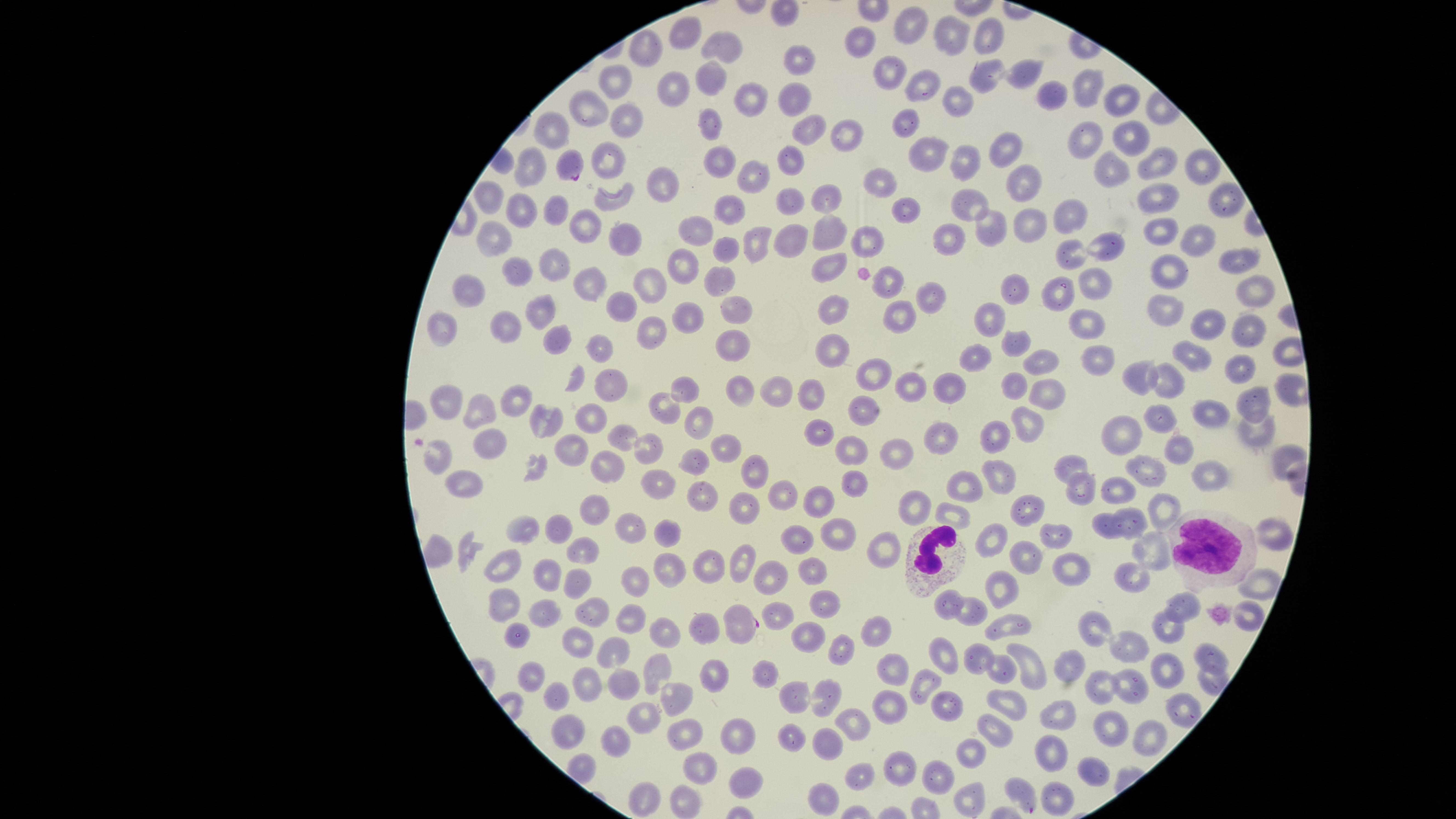

Approximate marker points as [x, y] in pixels.
Summary:
  - Parasitized RBCs: [565, 169], [741, 623]
  - Uninfected RBCs: [912, 22], [682, 33], [952, 35], [987, 35], [725, 39], [867, 41], [646, 50], [801, 56], [897, 71], [1026, 74], [985, 77], [711, 78], [619, 80], [920, 82], [674, 85], [1083, 91], [753, 95], [793, 96], [1054, 96], [1124, 98], [955, 100], [591, 107], [623, 115], [712, 123], [909, 123], [806, 129], [846, 130], [552, 134], [1087, 137], [1126, 137], [1005, 145], [925, 152], [608, 157], [789, 157], [723, 159], [963, 161], [1150, 163], [533, 164], [1108, 166], [1192, 166], [753, 174], [882, 177], [667, 184], [1022, 184], [1219, 193], [793, 194], [490, 197], [1156, 197], [908, 199], [618, 200], [731, 202], [826, 202], [970, 202], [527, 207], [1066, 212], [556, 218], [1028, 221], [586, 223], [990, 224], [695, 229], [828, 231], [953, 231], [1161, 231], [873, 234], [754, 237], [627, 238], [795, 239], [1197, 241], [497, 242], [1108, 243], [725, 248], [1072, 250], [1238, 257], [548, 265], [680, 265], [829, 266], [1167, 266], [515, 268], [719, 279], [888, 280], [591, 282], [652, 282], [1095, 283], [474, 287], [1023, 287], [1060, 288], [1252, 288], [930, 292], [624, 301], [834, 302], [730, 304], [1165, 308], [689, 310], [895, 310], [542, 315], [506, 317], [998, 317], [1089, 320], [1206, 320], [441, 324], [1246, 324], [651, 333], [563, 338], [734, 339], [1014, 345], [607, 347], [833, 347], [977, 352], [1193, 352], [1097, 354], [1042, 361], [1237, 366], [872, 372], [1135, 374], [571, 381], [1170, 383], [906, 384], [954, 384], [606, 385], [688, 385], [817, 385], [1015, 385], [739, 389], [781, 392], [1047, 394], [515, 399], [1258, 401], [446, 402], [661, 404], [1212, 407], [482, 408], [866, 408], [1156, 417], [1026, 418], [702, 419], [593, 421], [543, 422], [1121, 427], [1261, 429], [819, 433], [1000, 433], [948, 435], [627, 436], [852, 442], [488, 443], [726, 445], [1183, 446], [646, 448], [897, 448], [571, 449], [435, 458], [1282, 458], [1069, 459], [608, 463], [697, 464], [1145, 470], [760, 473], [1000, 476], [463, 478], [853, 478], [1211, 478], [1123, 480], [661, 483], [964, 483], [1085, 485], [701, 491], [818, 493], [785, 497], [918, 502], [742, 504], [1161, 508], [1026, 510], [597, 511], [955, 513], [1105, 520], [1131, 520], [631, 522], [552, 525], [666, 525], [520, 526], [795, 529], [840, 529], [1056, 534], [994, 537], [1272, 539], [437, 545], [892, 548], [576, 550], [1149, 551], [1026, 554], [744, 559], [505, 567], [707, 567], [815, 567], [1071, 569], [669, 572], [544, 574], [1133, 575], [772, 577], [574, 579], [637, 580], [1261, 584], [1001, 586], [829, 599], [951, 601], [505, 603], [974, 603], [1182, 604], [543, 610], [590, 610], [779, 613], [1247, 615], [633, 619], [704, 621], [1009, 624], [1094, 625], [1167, 626], [871, 627], [664, 629], [515, 636], [804, 636], [579, 639], [1133, 645], [837, 646], [944, 650], [611, 652], [974, 652], [1208, 655], [1033, 660], [661, 667], [1070, 668], [1170, 668], [893, 670], [998, 670], [535, 671], [709, 676], [761, 676], [1205, 681], [590, 683], [623, 683], [923, 684], [1131, 686], [1100, 688], [789, 692], [561, 695], [674, 695], [825, 695], [1009, 702], [950, 705], [1182, 706], [893, 710], [1056, 712], [640, 715], [1106, 725], [853, 730], [989, 730], [572, 732], [789, 732], [1145, 732], [686, 733], [740, 736], [618, 745], [827, 751], [970, 752], [1054, 752], [698, 769], [901, 772], [942, 772], [1093, 772], [862, 776], [745, 778], [1020, 785], [653, 795], [823, 796], [1056, 796], [685, 799], [972, 799]
  - WBCs: [1205, 541], [935, 555]
  - Field of view: single
  - Species: Plasmodium falciparum
  - Image size: 1456×819 pixels
  - Capture: smartphone photograph through the microscope eyepiece
  - Preparation: thin smear of blood
  - Presence: malaria parasites seen
  - Visible region: circular
  - Stain: Giemsa